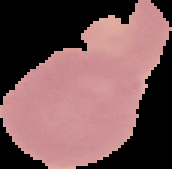
Image is 172×169 pixels. Malaria status: uninfected. Cell region segmented out of the field of view; the surrounding area is masked to black. From a thin blood film.